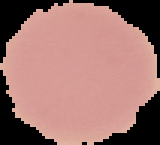

Summary:
  - Image type: cell region segmented out of the field of view; surrounding area masked to black
  - Preparation: thin blood smear
  - Result: no malaria parasites detected
  - Image size: 160×145 pixels